Classify this cell by malaria status.
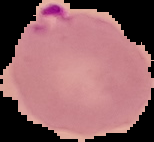

Parasitized.

Image is 154×142 pixels. Segmented cell region on a black background. From a thin blood film.